Describe the morphology of the erythrocytes.
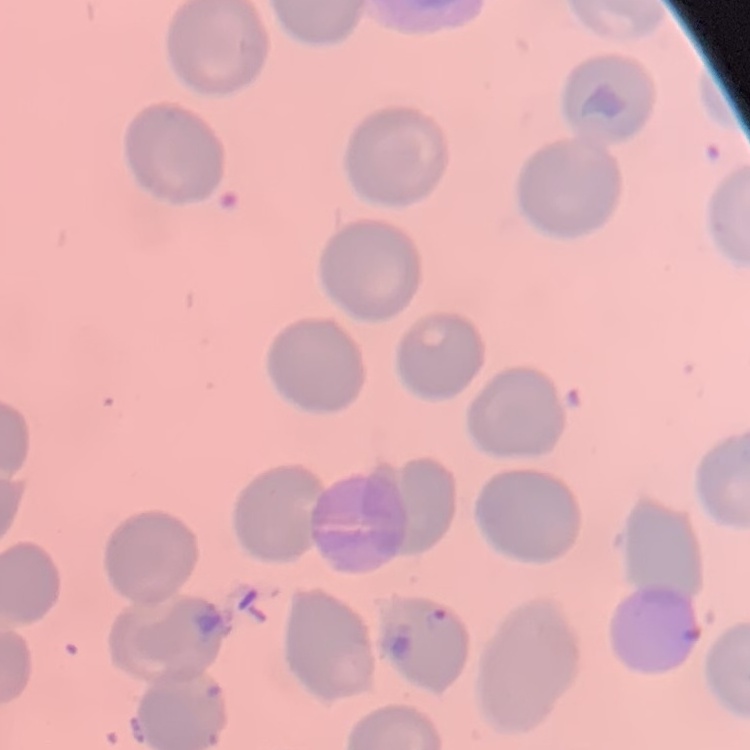

No rouleaux formation.

One tile cut from a larger photomicrograph. Thin peripheral smear. Stained with either Field's or Giemsa.